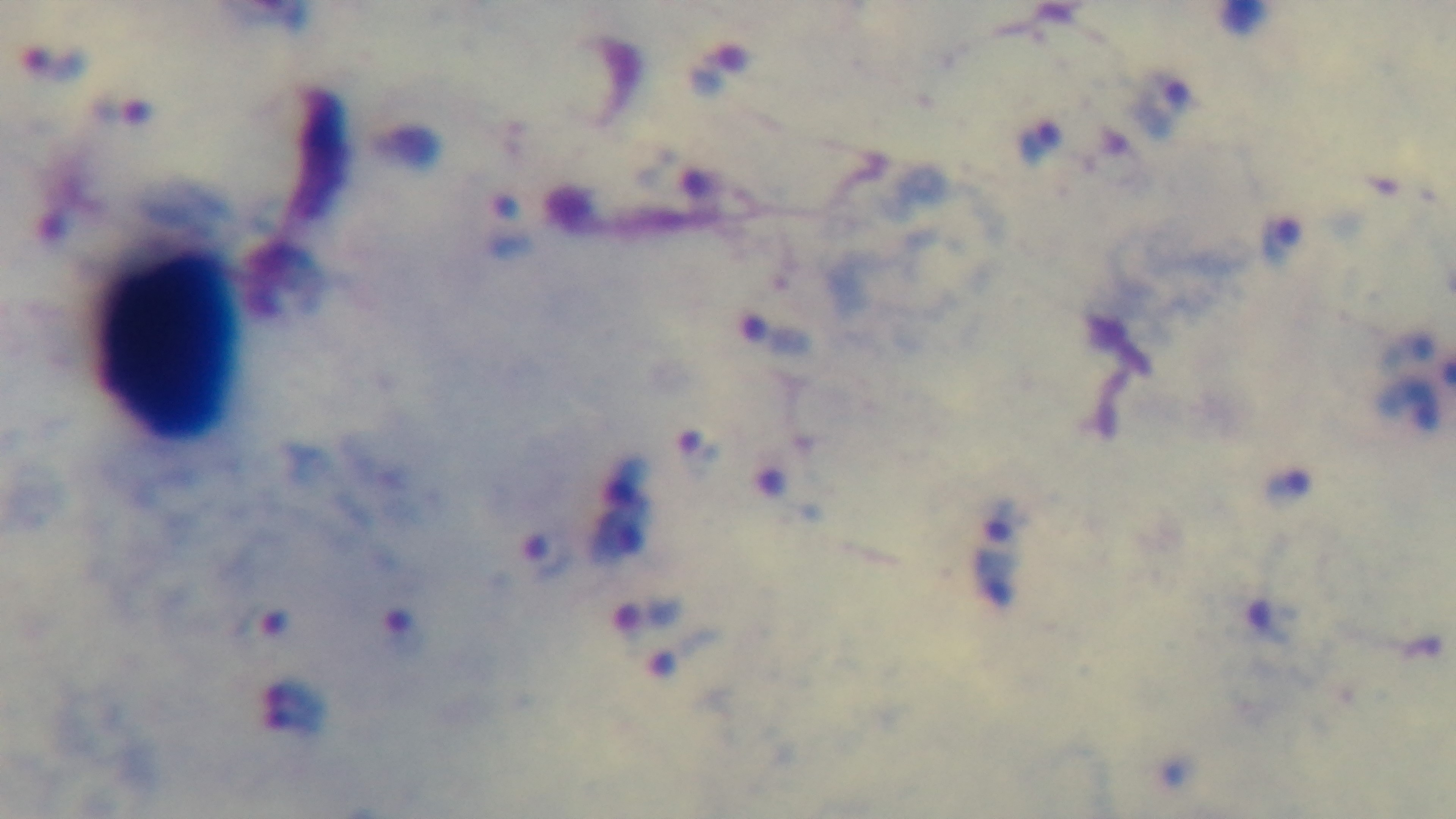

Summary:
  - Field of view: single
  - Stain: Giemsa
  - Preparation: thick blood film
  - Malaria status: positive
  - Objective: 100x oil immersion
  - Capture: mounted 4K digital camera
  - Modality: light microscopy